Identify the parasite.
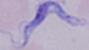
This is a trypanosome.

Summary:
  - Modality: micrograph
  - Magnification: 1000x